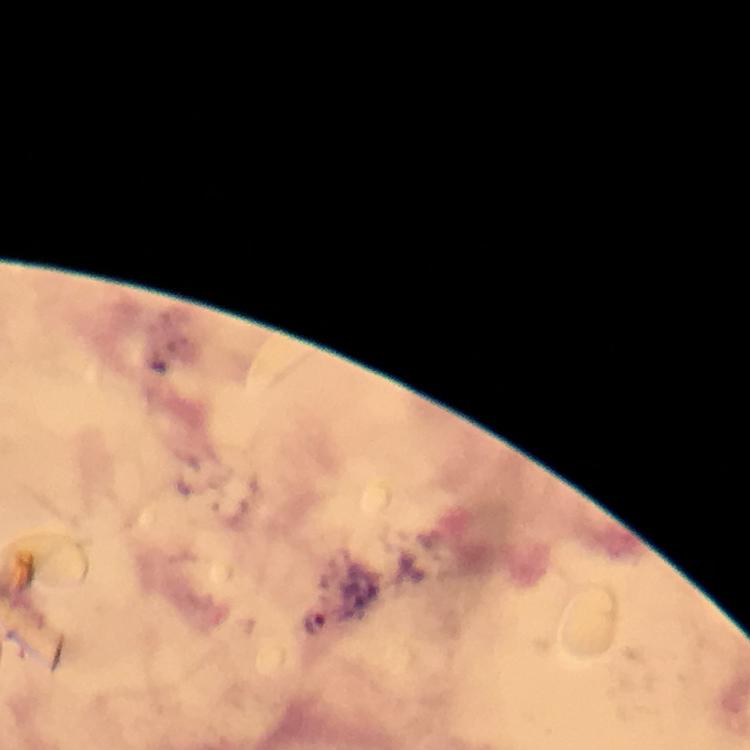
magnification = 100x
preparation = thick blood smear
Plasmodium parasite locations = approximate object centers, in pixels from the top-left corner: (x=314, y=621)
image size = 750×750 pixels
stain = Giemsa
capture = smartphone mounted on the microscope
cropped from = a single field of view
immersion oil = applied
context = from a malaria diagnostic workup